Give a bounding box for every artifact (platelet-like body, stain precipitate, or debris).
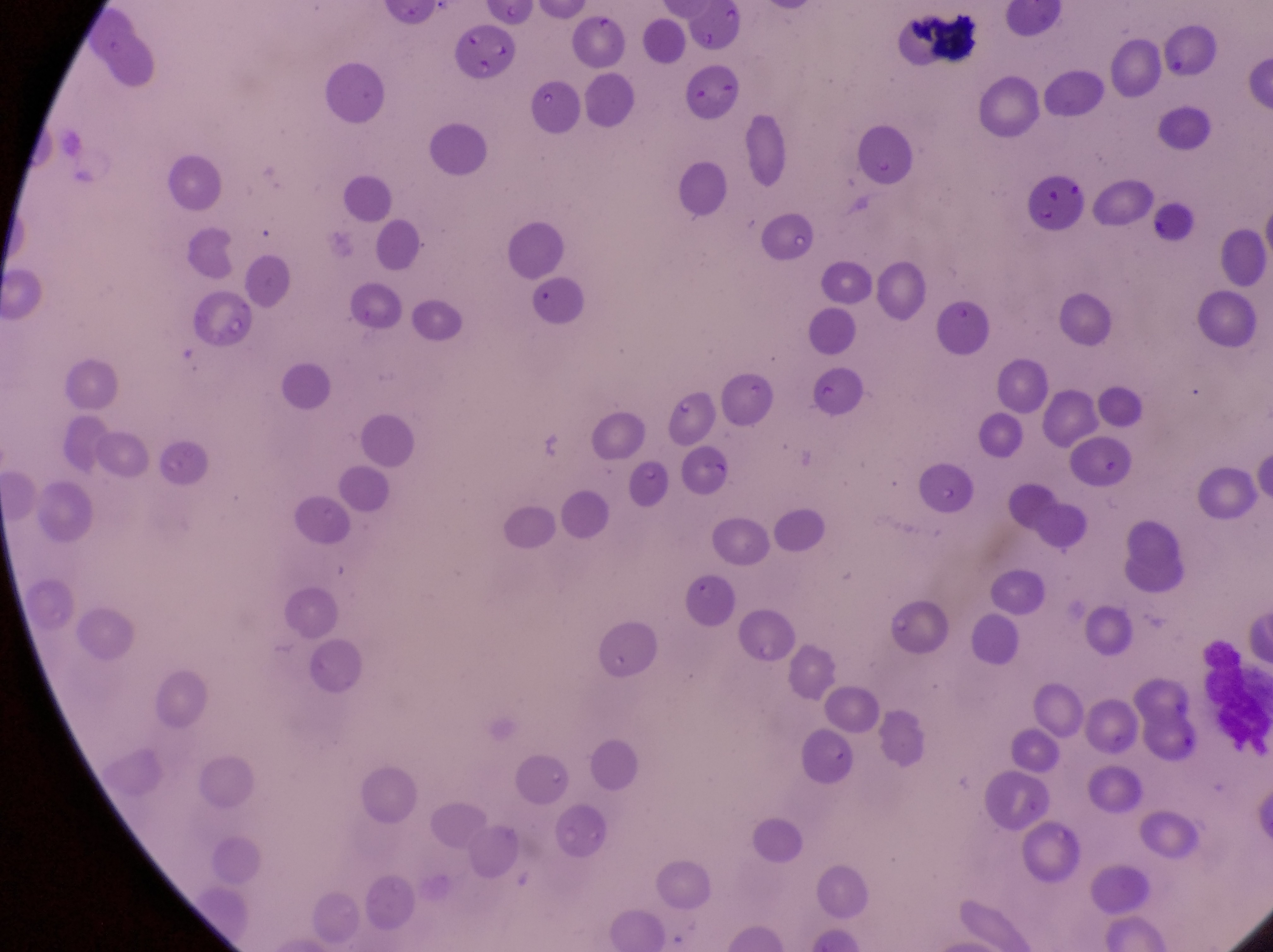
Approximate bounding boxes as [left, top, right, bottom] in pixels.
One object is labeled both leukocyte and artifact (platelet-like body, stain precipitate, or debris) by the source: [906, 7, 986, 74].

{
  "parasitised_red_blood_cell_locations": "approximate bounding boxes as [left, top, right, bottom] in pixels: [449, 20, 516, 77]",
  "country": "Uganda",
  "preparation": "thin blood smear",
  "magnification": "1000x",
  "image_size": "1273×952 pixels",
  "capture": "smartphone photograph through the eyepiece of an Olympus CX-23 microscope",
  "field_of_view": "single",
  "leukocyte_locations": "approximate bounding boxes as [left, top, right, bottom] in pixels: [1194, 640, 1270, 752]"
}